Name the blood parasite species.
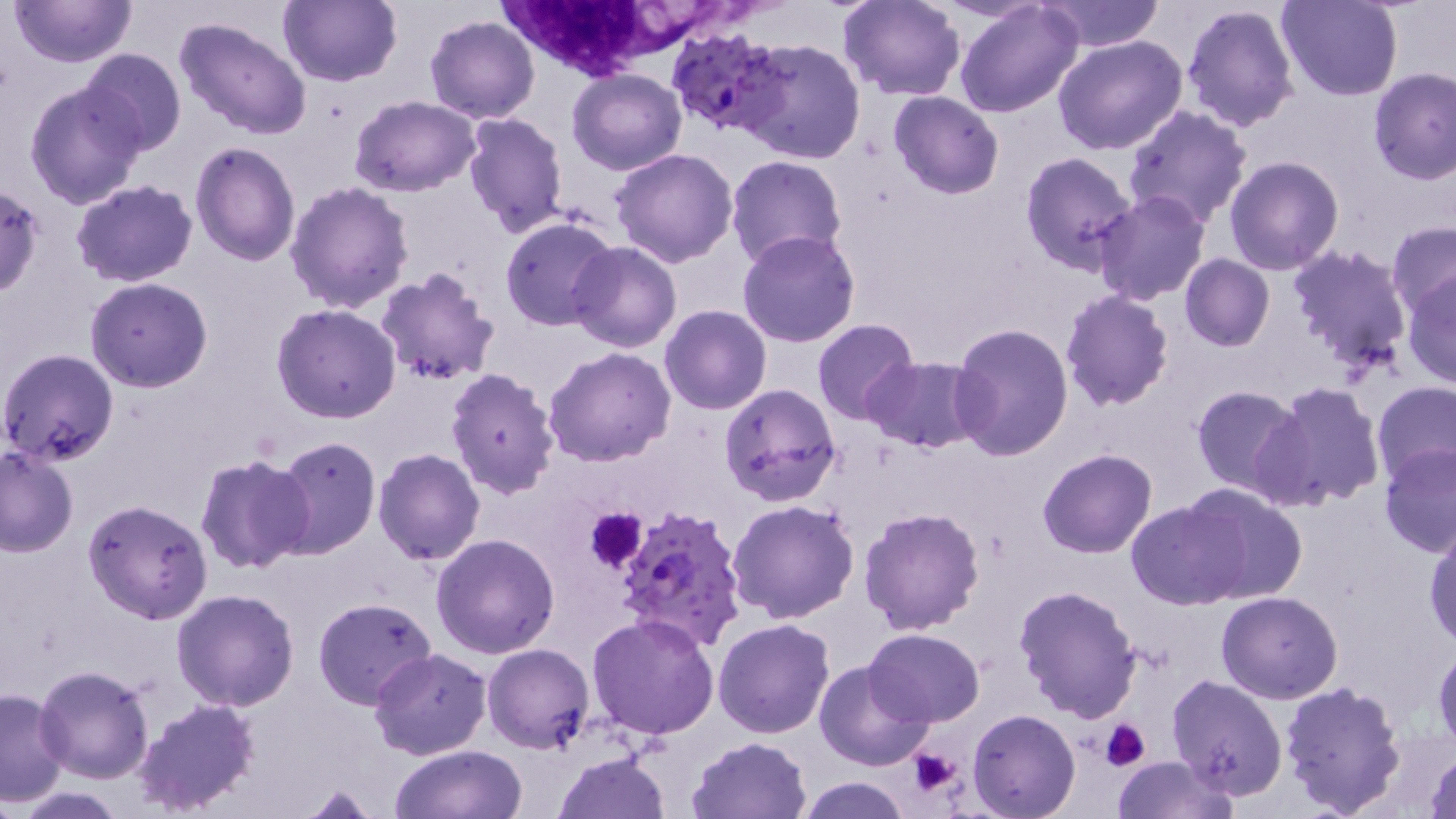
Plasmodium falciparum.

Approximate bounding boxes as [x1, y1, x2, y2] in pixels. Uninfected red blood cell locations: [9, 0, 135, 68], [279, 0, 401, 87], [837, 0, 966, 100], [1042, 0, 1163, 53], [1276, 0, 1404, 101], [954, 1, 1083, 118], [1181, 2, 1301, 135], [174, 15, 313, 141], [426, 17, 539, 123], [1053, 34, 1187, 155], [734, 39, 866, 165], [79, 48, 185, 157], [1368, 68, 1456, 184], [568, 69, 687, 175], [24, 79, 147, 209], [888, 90, 1003, 200], [351, 96, 478, 197], [1124, 105, 1252, 227], [462, 113, 568, 238], [190, 142, 300, 266], [611, 147, 739, 268], [1019, 153, 1139, 275], [726, 155, 847, 267], [1224, 156, 1344, 275], [70, 180, 198, 287], [285, 182, 414, 315], [0, 184, 44, 300], [1093, 190, 1211, 307], [499, 217, 618, 331], [1387, 220, 1456, 320], [736, 231, 860, 348], [567, 241, 681, 352], [1288, 242, 1415, 383], [1180, 254, 1274, 352], [374, 268, 499, 387], [1403, 274, 1455, 387], [86, 277, 213, 392], [1060, 289, 1175, 410], [271, 304, 401, 423], [660, 306, 772, 415], [812, 320, 920, 425], [950, 322, 1073, 461], [543, 346, 675, 465], [0, 348, 119, 465], [862, 357, 984, 453], [444, 366, 560, 499], [1372, 380, 1456, 486], [1266, 381, 1385, 510], [719, 383, 841, 505], [1190, 384, 1308, 498], [272, 435, 382, 559], [1379, 443, 1456, 557], [0, 445, 80, 558], [374, 448, 486, 565], [1038, 449, 1156, 559], [196, 453, 315, 575], [1186, 483, 1307, 604], [82, 499, 215, 625], [1127, 499, 1247, 610], [727, 500, 860, 624], [858, 506, 985, 634], [1425, 523, 1456, 649], [431, 534, 559, 659], [1015, 584, 1143, 723], [171, 589, 299, 712], [1216, 590, 1343, 703], [313, 596, 435, 708], [586, 613, 720, 739], [714, 618, 835, 737], [864, 628, 985, 726], [483, 642, 594, 753], [1433, 644, 1455, 753], [371, 650, 491, 760], [814, 660, 932, 770], [33, 665, 157, 784], [1167, 674, 1289, 797], [1276, 679, 1407, 818], [0, 689, 71, 805], [130, 697, 260, 817], [968, 707, 1083, 819], [687, 736, 812, 818], [390, 745, 528, 819], [1424, 748, 1456, 819], [554, 749, 671, 819], [1111, 755, 1238, 818], [794, 776, 913, 819], [286, 784, 385, 818]. White blood cell locations: [496, 0, 685, 72]. Platelet locations: [586, 508, 647, 572], [1100, 720, 1151, 771], [906, 749, 961, 798]. Plasmodium falciparum-infected red blood cell locations: [663, 27, 786, 138], [614, 503, 750, 653]. Single field of view. Thin blood smear. Light microscopy. Image is 1456×819 pixels. May-Grünwald-Giemsa-stained preparation. 1000x magnification.